Report the malaria status.
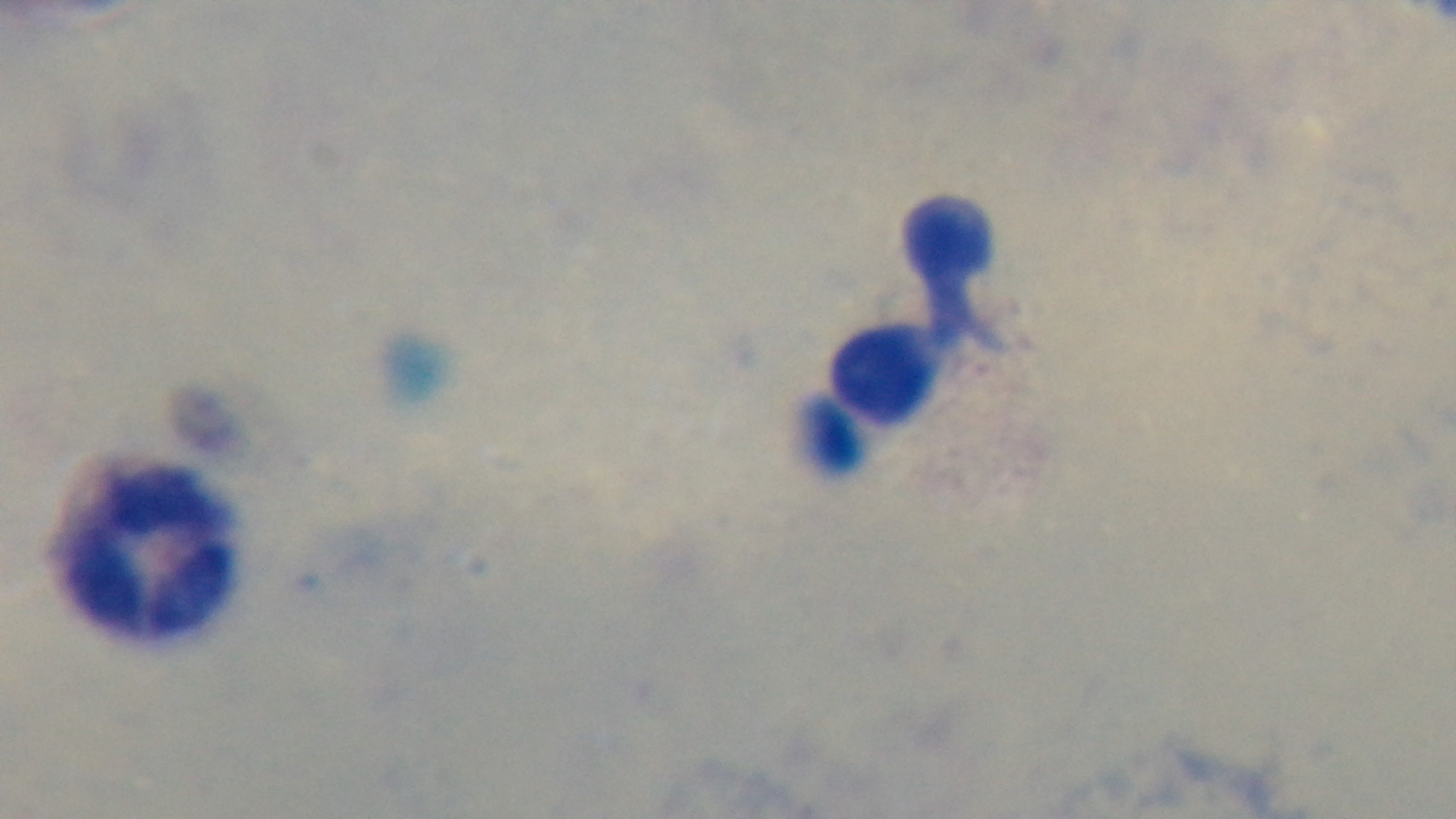
Negative.

Summary:
  - Capture: mounted 4K digital camera
  - Field of view: one from the slide
  - Preparation: thick blood film
  - Modality: light microscopy
  - Objective: 100x oil immersion
  - Stain: Giemsa